State which parasite is depicted.
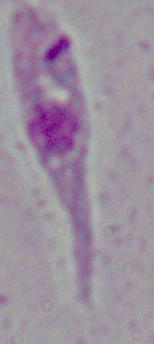

This is Leishmania.

modality = photomicrograph
magnification = 1000x